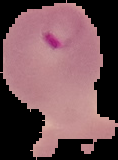

From a thin blood smear. Malaria status: parasitized. Image is 118×160 pixels. The area outside the segmented cell region is set to black.